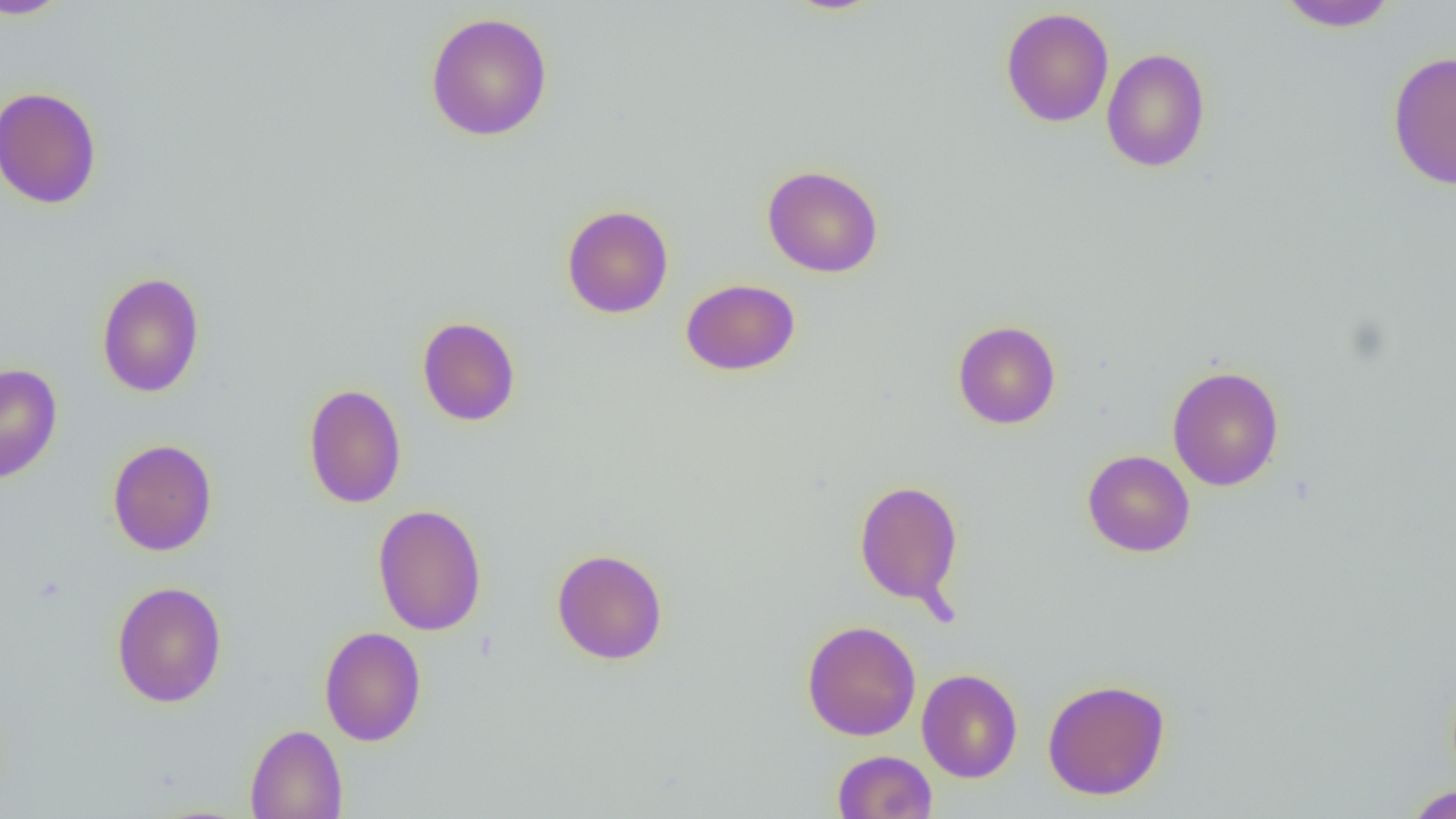

Summary:
  - Coordinate format: approximate bounding boxes as (x1,y1)-(x2,y2) corner pairs in pixels
  - Uninfected red blood cell locations: (0,0)-(73,20), (1275,0)-(1400,32), (1000,7)-(1114,128), (425,12)-(553,141), (1101,48)-(1211,172), (1387,51)-(1456,190), (0,86)-(102,210), (762,164)-(884,278), (561,204)-(674,318), (96,272)-(205,398), (680,278)-(800,376), (417,316)-(521,427), (952,320)-(1061,429), (0,363)-(62,484), (1167,365)-(1285,491), (303,383)-(407,509), (107,438)-(217,556), (1082,449)-(1196,558), (853,479)-(963,609), (372,503)-(487,636), (551,548)-(668,665), (112,581)-(227,708), (801,620)-(921,741), (318,626)-(427,746), (916,668)-(1023,783), (1042,678)-(1171,800), (244,724)-(348,819), (832,750)-(937,818), (1404,785)-(1456,818)
  - Slide-level diagnosis: negative for blood parasites
  - Modality: light microscopy
  - Magnification: 1000x
  - Field of view: single
  - Preparation: thin blood smear
  - Image size: 1456×819 pixels